Outline platelets.
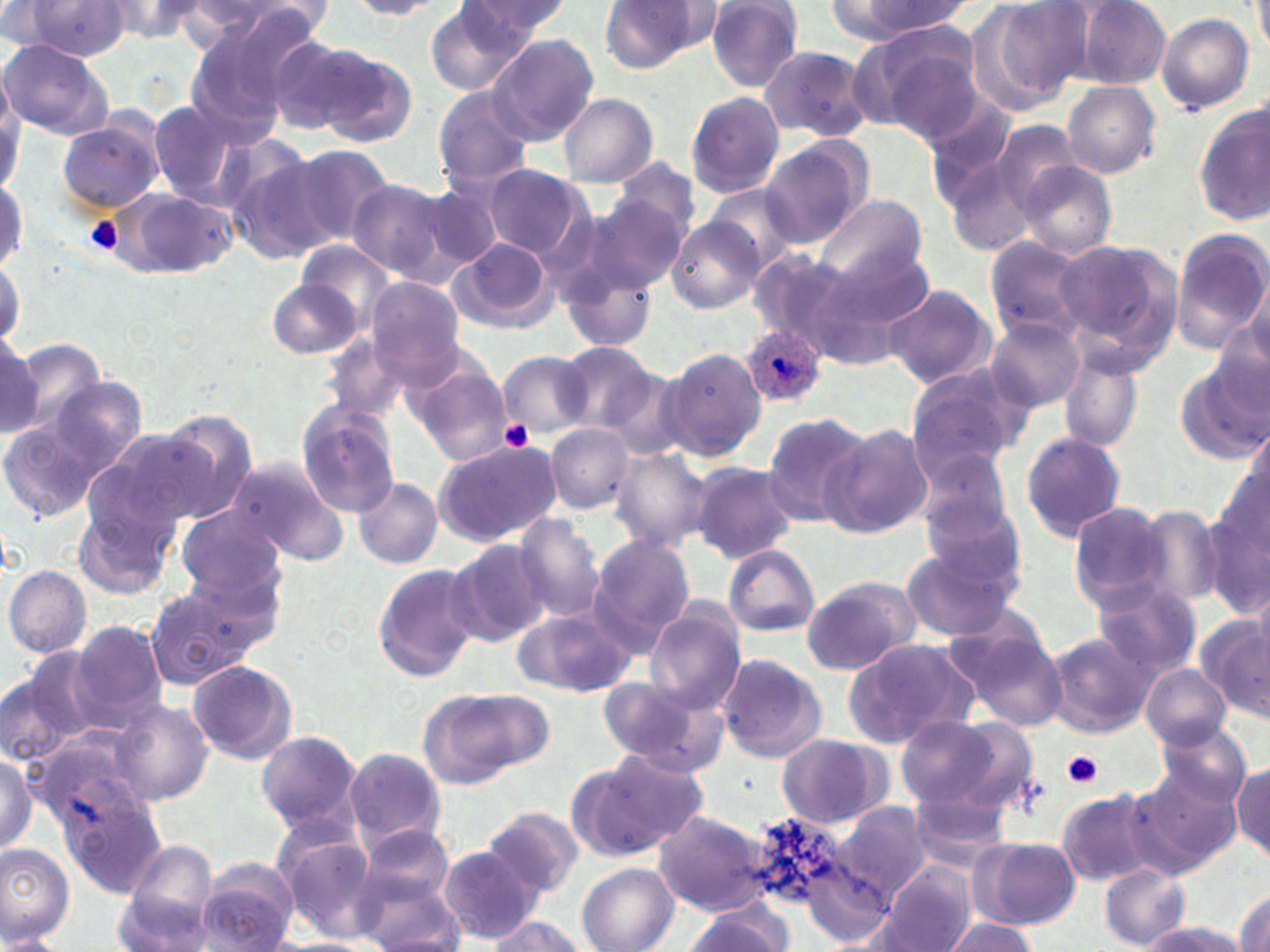

Approximate bounding boxes as [x1, y1, x2, y2] in pixels.
Platelets: [85, 216, 124, 254], [499, 420, 535, 450], [1063, 751, 1103, 789].

Summary:
  - Uninfected red blood cell locations: [706, 0, 803, 91], [970, 0, 1089, 112], [1252, 0, 1270, 54], [97, 1, 213, 44], [174, 1, 312, 46], [348, 1, 452, 19], [458, 1, 574, 41], [600, 1, 708, 74], [839, 1, 972, 40], [1071, 1, 1171, 88], [18, 2, 134, 59], [423, 2, 540, 98], [1155, 12, 1255, 114], [864, 27, 986, 142], [181, 28, 300, 147], [487, 33, 599, 145], [266, 34, 369, 134], [1, 40, 112, 139], [759, 45, 872, 142], [314, 48, 416, 147], [1062, 80, 1161, 179], [434, 85, 535, 191], [685, 90, 785, 200], [559, 92, 657, 187], [921, 93, 1020, 203], [148, 101, 238, 197], [1195, 106, 1270, 228], [56, 118, 164, 214], [989, 120, 1082, 211], [758, 138, 870, 248], [218, 140, 332, 258], [284, 143, 395, 250], [606, 156, 701, 253], [945, 158, 1042, 257], [1015, 160, 1118, 259], [482, 164, 587, 258], [0, 171, 27, 283], [346, 180, 455, 279], [416, 183, 507, 274], [706, 185, 800, 268], [110, 188, 239, 281], [589, 189, 692, 291], [815, 193, 926, 285], [667, 217, 766, 313], [1170, 229, 1270, 351], [451, 236, 556, 333], [1054, 237, 1184, 369], [298, 239, 395, 331], [984, 239, 1093, 344], [814, 244, 936, 353], [750, 248, 855, 350], [558, 250, 660, 356], [0, 252, 25, 350], [1247, 275, 1270, 367], [365, 276, 467, 384], [267, 278, 360, 359], [883, 283, 995, 388], [985, 317, 1086, 413], [1210, 320, 1270, 426], [0, 329, 41, 442], [8, 338, 107, 440], [558, 343, 660, 433], [661, 347, 766, 462], [498, 349, 594, 436], [1057, 350, 1144, 452], [1175, 360, 1268, 464], [409, 363, 513, 468], [600, 365, 696, 462], [904, 366, 1026, 482], [23, 373, 151, 506], [297, 404, 401, 517], [153, 410, 259, 522], [762, 412, 871, 528], [822, 422, 934, 538], [545, 424, 635, 515], [81, 429, 204, 546], [1020, 431, 1126, 543], [433, 440, 562, 547], [913, 445, 1014, 540], [607, 447, 709, 553], [225, 456, 349, 565], [688, 461, 799, 563], [354, 477, 442, 568], [1201, 492, 1270, 619], [74, 494, 176, 601], [1069, 501, 1172, 611], [920, 502, 1030, 602], [1130, 504, 1223, 607], [177, 507, 286, 603], [510, 515, 605, 623], [587, 534, 697, 654], [445, 539, 549, 647], [175, 543, 288, 661], [898, 543, 1023, 642], [723, 544, 821, 638], [371, 563, 483, 683], [5, 564, 92, 658], [801, 575, 919, 675], [1089, 578, 1203, 677], [1252, 578, 1270, 664], [144, 586, 258, 690], [514, 605, 638, 698], [644, 608, 745, 715], [1197, 613, 1270, 721], [948, 621, 1066, 730], [65, 622, 168, 736], [1044, 630, 1156, 736], [843, 636, 978, 748], [713, 653, 828, 763], [0, 656, 101, 768], [187, 659, 297, 766], [1142, 663, 1231, 749], [596, 676, 718, 768], [422, 687, 552, 785], [115, 698, 215, 805], [894, 718, 1008, 809], [1154, 725, 1250, 812], [255, 729, 361, 836], [775, 733, 889, 829], [35, 739, 165, 897], [344, 746, 447, 848], [578, 747, 708, 857], [0, 751, 37, 857], [1230, 761, 1270, 862], [1131, 763, 1242, 870], [905, 783, 1011, 872], [1056, 789, 1159, 885], [830, 801, 930, 903], [484, 806, 582, 897], [651, 809, 772, 915], [744, 812, 864, 921], [271, 823, 381, 938], [357, 824, 455, 912], [971, 836, 1079, 930], [0, 843, 75, 946], [439, 845, 542, 944], [196, 857, 300, 951], [801, 857, 898, 945], [113, 862, 220, 952], [874, 862, 975, 952], [578, 863, 679, 952], [1100, 865, 1190, 949], [354, 869, 465, 951], [1233, 889, 1270, 952], [682, 905, 787, 952], [484, 916, 588, 952], [944, 917, 1039, 952], [1138, 919, 1245, 952], [0, 934, 65, 952]
  - Plasmodium ovale-infected red blood cell locations: [741, 324, 827, 409]
  - Slide-level diagnosis: Plasmodium ovale
  - Modality: optical microscopy
  - Field of view: one of a larger specimen
  - Magnification: 1000x
  - Image size: 1270×952 pixels
  - Stain: May-Grünwald-Giemsa
  - Preparation: thin blood film